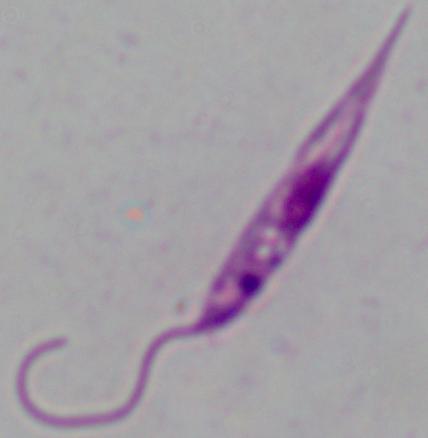

magnification = 1000x
identification = Leishmania
modality = micrograph